Comment on the morphology of the red blood cells.
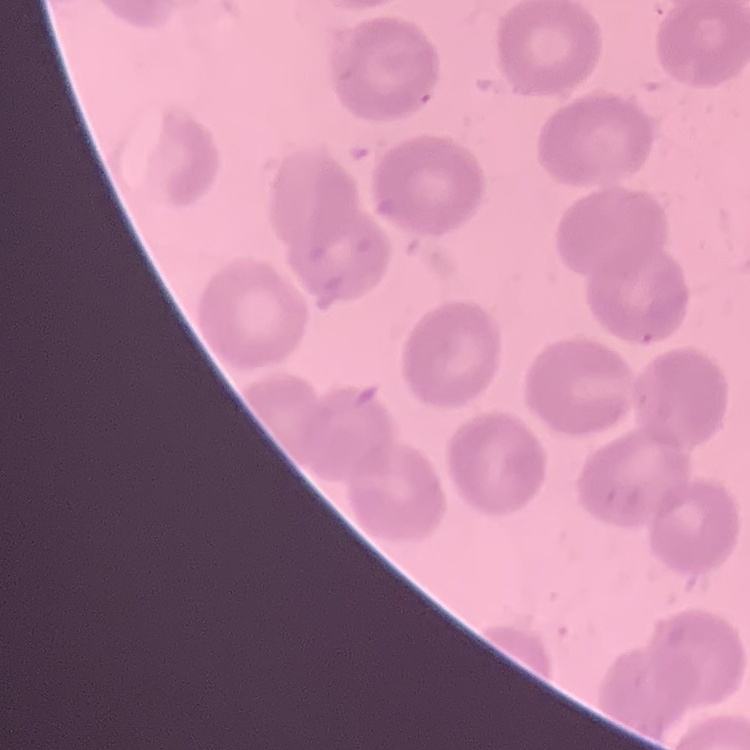

No rouleaux formation.

Stained with either Field's or Giemsa. One tile cut from a larger photomicrograph. Thin peripheral smear.